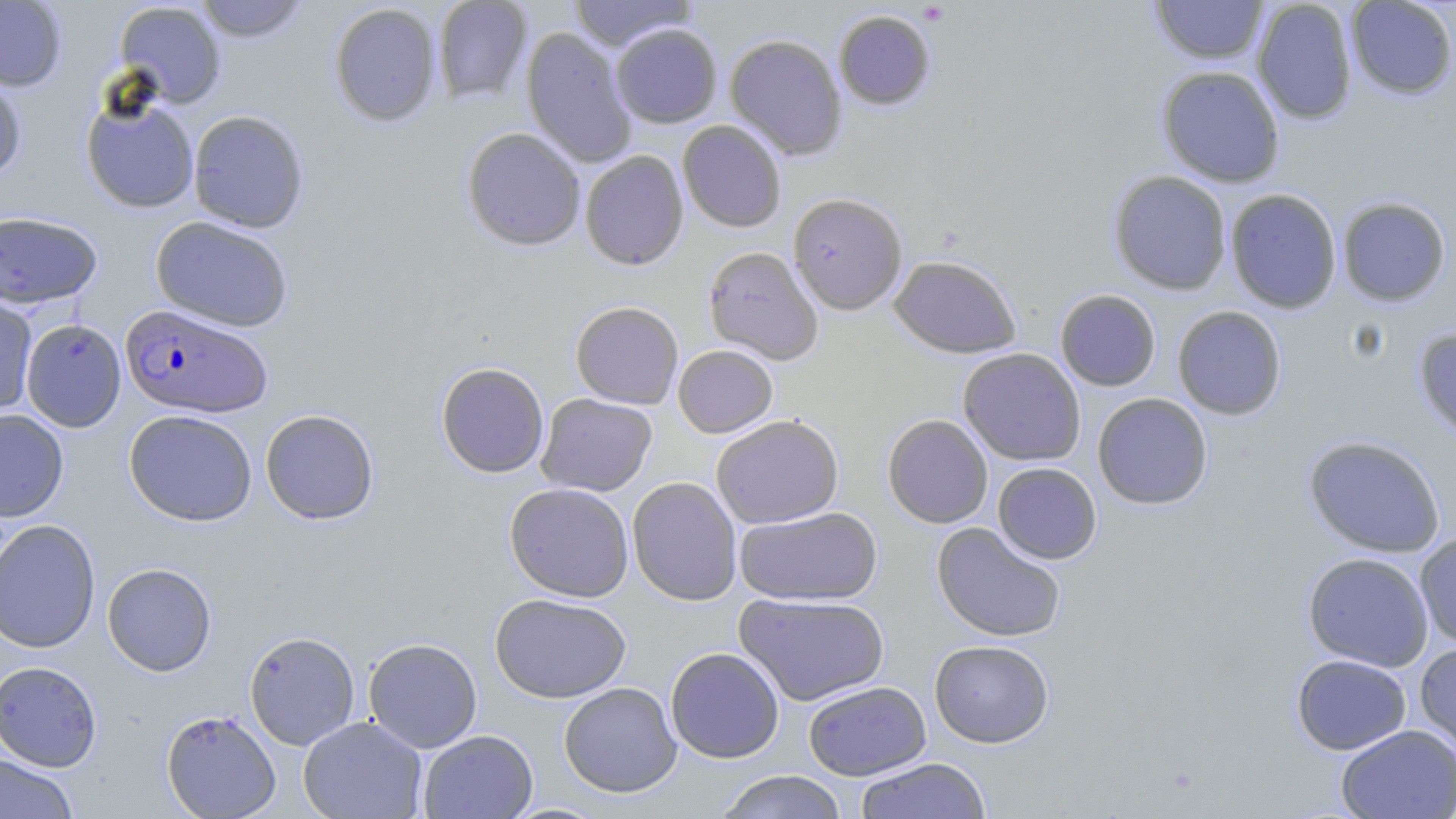

Approximate bounding boxes as (x1, y1, x2, y2) in pixels. Uninfected red blood cell locations: (0, 0, 67, 91), (192, 0, 311, 42), (432, 0, 533, 104), (567, 0, 697, 51), (1252, 0, 1358, 124), (1346, 0, 1456, 99), (1150, 1, 1268, 64), (114, 2, 226, 107), (329, 3, 442, 126), (833, 10, 936, 111), (610, 24, 722, 128), (521, 27, 637, 168), (724, 33, 847, 160), (1157, 65, 1285, 187), (0, 68, 27, 183), (80, 92, 200, 214), (188, 110, 309, 232), (677, 120, 786, 232), (461, 127, 586, 251), (580, 151, 689, 270), (1108, 170, 1232, 295), (1225, 188, 1342, 314), (788, 192, 908, 314), (1337, 196, 1451, 306), (0, 211, 102, 308), (151, 216, 294, 331), (703, 247, 824, 364), (888, 255, 1021, 358), (1055, 289, 1161, 391), (0, 295, 38, 418), (570, 301, 683, 409), (1172, 305, 1286, 420), (21, 319, 125, 431), (1414, 326, 1456, 443), (673, 345, 778, 438), (958, 348, 1086, 465), (436, 362, 549, 478), (1093, 392, 1212, 509), (536, 393, 657, 496), (0, 408, 69, 521), (124, 409, 258, 526), (260, 409, 379, 524), (711, 414, 844, 529), (882, 414, 993, 528), (1303, 435, 1447, 558), (993, 462, 1102, 564), (627, 477, 743, 606), (504, 482, 635, 602), (733, 505, 883, 606), (0, 519, 101, 653), (931, 522, 1066, 643), (1414, 532, 1456, 648), (1303, 552, 1434, 671), (102, 563, 216, 676), (734, 592, 891, 706), (490, 593, 632, 703), (244, 630, 360, 750), (363, 637, 483, 752), (929, 640, 1054, 747), (1414, 641, 1456, 761), (665, 647, 784, 763), (1291, 654, 1411, 755), (0, 660, 102, 771), (803, 681, 932, 780), (558, 682, 682, 797), (161, 709, 281, 818), (298, 715, 427, 819), (1336, 723, 1456, 819), (418, 729, 538, 819), (0, 753, 78, 819), (855, 758, 992, 819), (714, 770, 849, 819). Plasmodium falciparum-infected red blood cell locations: (120, 304, 272, 418). Slide-level diagnosis: Plasmodium falciparum. Light microscopy. Thin blood film. One field of a larger specimen. May-Grünwald-Giemsa-stained preparation. Image is 1456×819 pixels. Captured at 1000x magnification.